Outline each blood parasite and name the species.
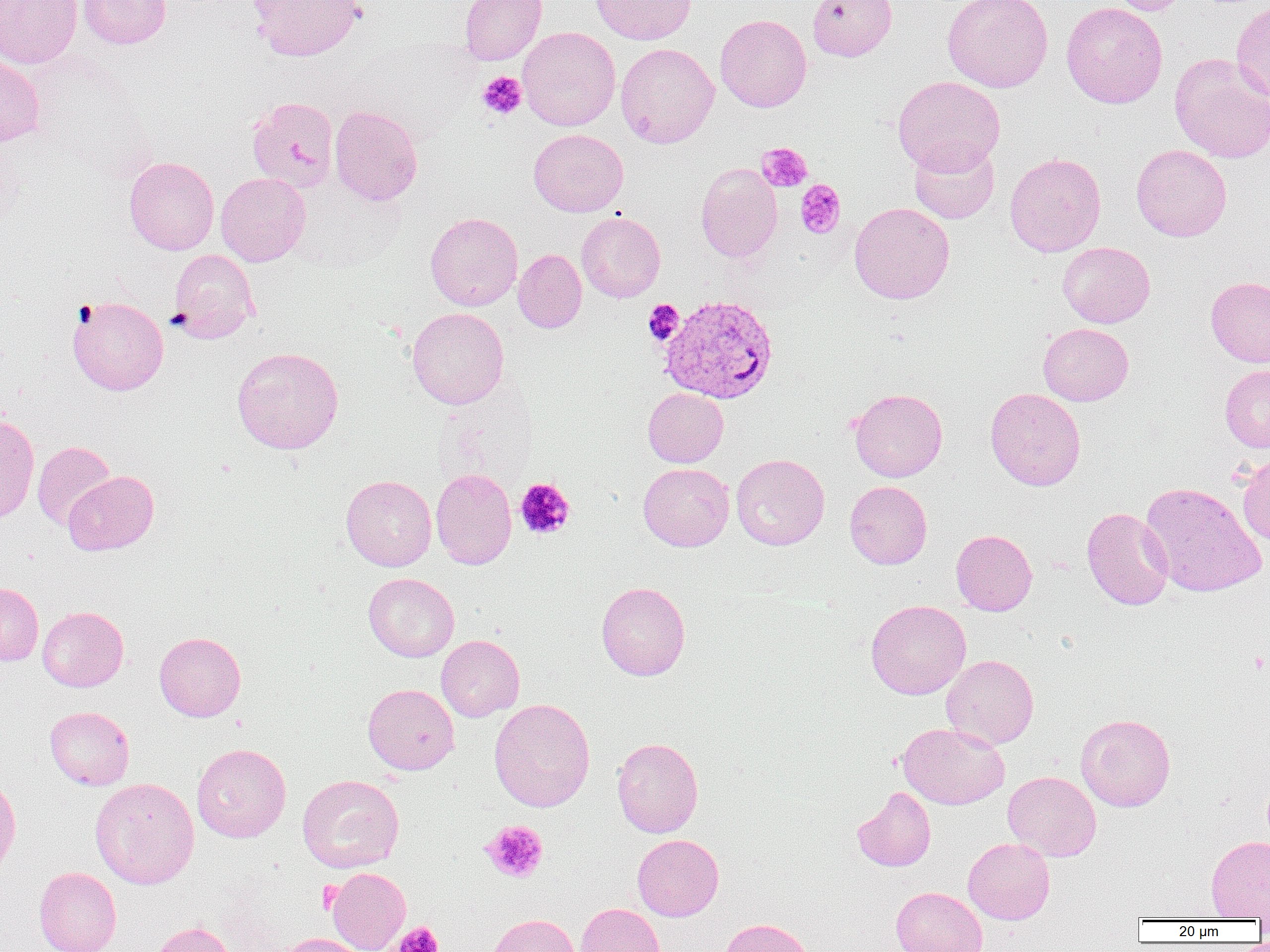

Approximate bounding boxes as (x1,y1)-(x2,y2) corner pairs in pixels.
Plasmodium vivax-infected red blood cells: (659,295)-(778,403).
No Plasmodium falciparum, Plasmodium ovale, Plasmodium malariae, Babesia divergens, or Trypanosoma brucei observed.

Summary:
  - Uninfected red blood cell locations: (0,0)-(82,69), (77,0)-(172,49), (248,0)-(364,61), (459,0)-(547,65), (591,0)-(697,44), (807,0)-(897,61), (942,0)-(1053,92), (1105,0)-(1190,15), (1061,2)-(1168,109), (1231,3)-(1270,103), (715,14)-(812,112), (517,26)-(620,131), (615,42)-(719,148), (0,53)-(45,147), (1169,53)-(1270,164), (893,75)-(1005,174), (246,96)-(339,192), (329,105)-(423,206), (529,129)-(628,217), (909,139)-(999,224), (1131,144)-(1232,241), (1004,152)-(1106,257), (124,156)-(219,255), (695,163)-(782,263), (216,172)-(311,266), (849,202)-(954,304), (425,212)-(523,310), (576,212)-(665,302), (1057,241)-(1155,328), (168,249)-(259,343), (514,249)-(587,332), (1206,276)-(1270,367), (67,295)-(168,395), (407,307)-(509,409), (1038,323)-(1133,406), (231,346)-(344,454), (1220,365)-(1270,452), (985,387)-(1086,490), (643,388)-(728,467), (849,388)-(948,482), (0,414)-(40,523), (32,440)-(116,530), (731,453)-(830,550), (1237,454)-(1270,546), (638,463)-(734,551), (431,468)-(517,569), (63,470)-(159,555), (341,475)-(437,571), (845,481)-(932,569), (1140,482)-(1267,598), (1081,507)-(1174,610), (951,529)-(1037,615), (363,572)-(459,662), (0,582)-(43,666), (596,582)-(691,680), (866,600)-(971,699), (38,606)-(128,692), (154,631)-(246,721), (436,635)-(524,721), (942,655)-(1039,749), (362,683)-(459,774), (489,698)-(595,812), (45,706)-(134,790), (1076,713)-(1175,811), (898,722)-(1009,809), (612,737)-(703,838), (191,743)-(291,842), (1003,771)-(1101,861), (0,774)-(21,878), (297,774)-(404,872), (90,777)-(200,889), (852,786)-(936,872), (632,834)-(724,921), (1206,835)-(1270,919), (963,837)-(1055,924), (34,866)-(121,952), (326,866)-(410,952), (891,886)-(987,952), (576,903)-(666,952), (485,913)-(582,952), (718,918)-(815,952), (149,921)-(233,952), (273,933)-(369,952)
  - Platelet locations: (476,71)-(526,120), (756,142)-(813,193), (795,179)-(846,238), (644,300)-(684,346), (515,478)-(575,540), (481,820)-(548,883), (317,881)-(343,912), (394,922)-(443,952)
  - Slide-level diagnosis: Plasmodium vivax
  - Modality: light microscopy
  - Magnification: 1000x
  - Image size: 1270×952 pixels
  - Preparation: thin blood smear
  - Field of view: one of a larger specimen